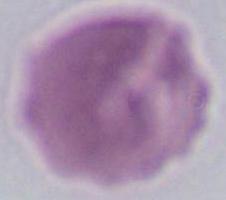
Photomicrograph. Captured at 1000x magnification. An erythrocyte is seen.